Classify this cell by malaria status.
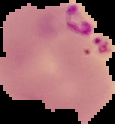

It is parasitized.

image type = segmented cell region with the area outside set to black
image size = 115×124 pixels
preparation = thin blood film